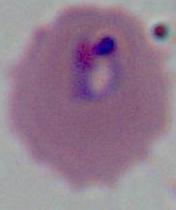

modality = micrograph
magnification = 400x or 1000x
identification = Plasmodium